Give the position of every Plasmodium parasite and every leukocyte.
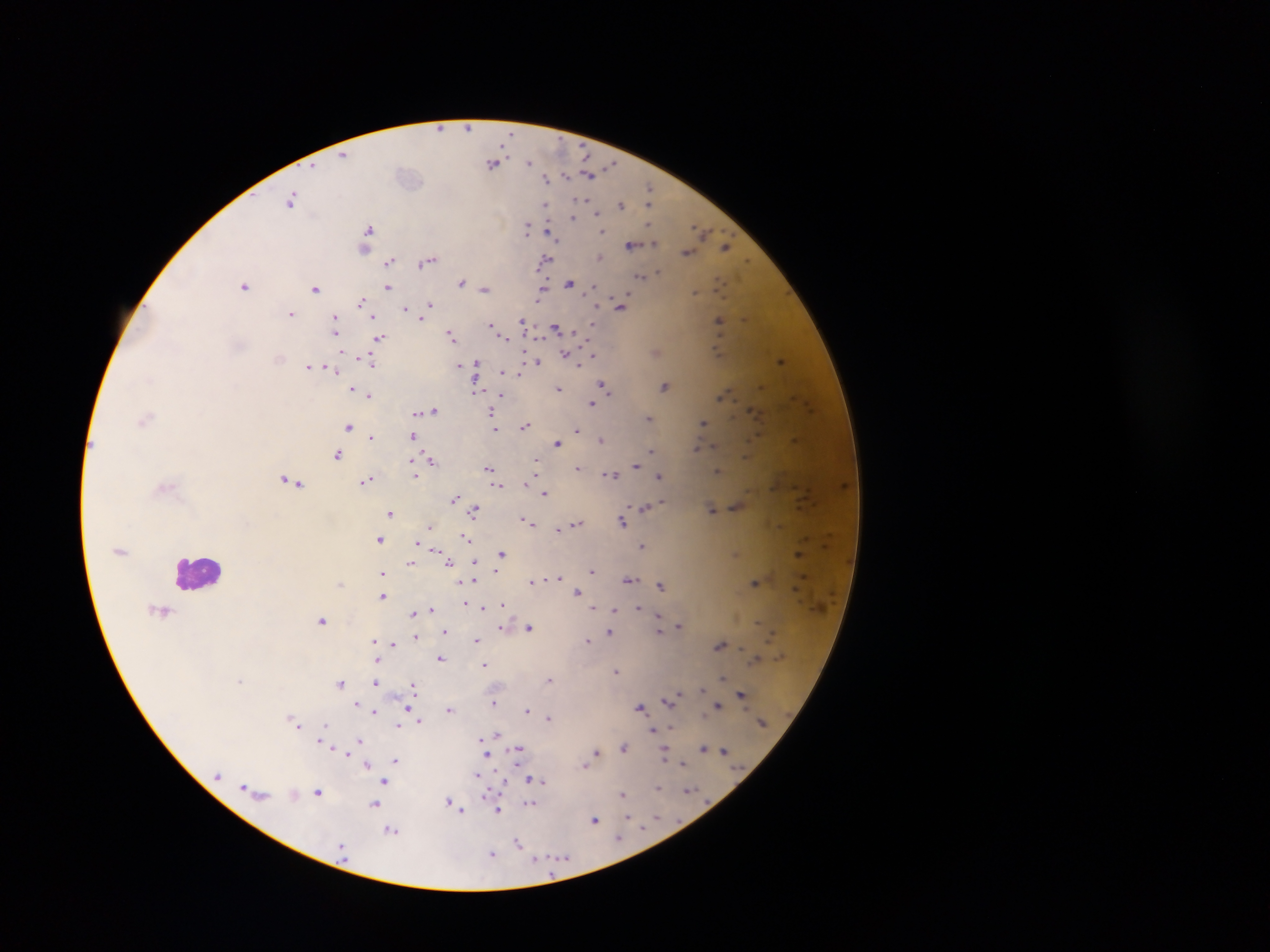

Approximate centers as [x, y] in pixels.
Plasmodium parasites: [440, 127], [468, 127], [344, 154], [530, 162], [494, 163], [590, 174], [567, 177], [547, 178], [650, 189], [649, 197], [291, 200], [621, 203], [546, 205], [651, 205], [597, 212], [574, 216], [528, 227], [368, 231], [603, 231], [702, 231], [551, 233], [632, 245], [365, 246], [727, 247], [688, 252], [600, 257], [428, 260], [545, 260], [389, 262], [659, 272], [641, 275], [462, 281], [570, 283], [245, 285], [388, 287], [316, 288], [486, 288], [542, 289], [592, 289], [695, 292], [362, 301], [430, 304], [621, 304], [406, 308], [291, 313], [422, 318], [746, 318], [336, 319], [719, 320], [524, 321], [593, 323], [491, 324], [556, 328], [337, 331], [452, 335], [502, 335], [379, 337], [567, 354], [591, 355], [279, 358], [781, 359], [371, 360], [536, 362], [477, 363], [580, 363], [460, 364], [308, 366], [331, 369], [502, 371], [520, 376], [665, 385], [603, 386], [352, 388], [559, 388], [476, 389], [368, 395], [723, 396], [592, 402], [434, 410], [491, 413], [649, 417], [144, 419], [703, 422], [349, 425], [526, 425], [495, 429], [577, 430], [413, 435], [370, 436], [796, 439], [601, 440], [558, 441], [713, 446], [696, 447], [653, 450], [337, 454], [747, 455], [430, 459], [536, 460], [536, 465], [636, 465], [489, 468], [578, 468], [719, 469], [612, 474], [415, 475], [659, 475], [366, 480], [291, 481], [497, 485], [545, 491], [455, 498], [459, 502], [662, 502], [656, 504], [736, 505], [645, 506], [712, 509], [475, 510], [391, 512], [526, 520], [622, 520], [577, 523], [565, 526], [431, 527], [560, 527], [467, 537], [379, 539], [417, 542], [642, 546], [501, 553], [799, 553], [475, 561], [450, 562], [412, 563], [497, 569], [592, 570], [382, 573], [559, 577], [630, 580], [532, 581], [474, 582], [756, 582], [340, 583], [660, 584], [577, 591], [382, 595], [465, 604], [502, 604], [483, 607], [638, 607], [432, 608], [593, 608], [615, 608], [162, 610], [414, 613], [658, 615], [323, 620], [659, 622], [757, 623], [679, 626], [501, 627], [529, 628], [660, 629], [445, 630], [609, 632], [417, 636], [476, 640], [588, 640], [375, 641], [393, 644], [720, 644], [441, 657], [756, 658], [376, 660], [484, 665], [616, 671], [724, 677], [241, 679], [550, 679], [376, 682], [340, 683], [413, 685], [703, 689], [742, 694], [671, 699], [495, 702], [357, 703], [717, 705], [640, 707], [450, 708], [407, 709], [528, 709], [375, 711], [549, 718], [420, 721], [297, 725], [327, 725], [399, 726], [671, 727], [653, 730], [497, 733], [360, 740], [322, 741], [481, 741], [625, 747], [704, 747], [519, 749], [725, 750], [597, 751], [345, 752], [665, 753], [487, 756], [396, 760], [684, 763], [367, 764], [584, 765], [478, 774], [480, 777], [532, 778], [539, 779], [386, 780], [502, 780], [658, 788], [688, 790], [319, 791], [294, 794], [623, 794], [449, 801], [531, 803], [375, 804], [455, 804], [459, 809], [498, 809], [628, 816], [656, 816], [595, 820], [393, 831], [620, 837], [518, 842], [492, 854], [536, 858].
Leukocytes: [199, 572].

Mobile-phone photograph taken through the microscope. Thick blood smear. Single field of view. Collected in Ghana. Image is 1270×952 pixels.